Report the malaria status of this cell.
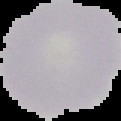
It is uninfected.

preparation = thin blood smear
image type = cell region segmented out of the field of view; surrounding area masked to black
image size = 121×121 pixels